Point out each malaria parasite.
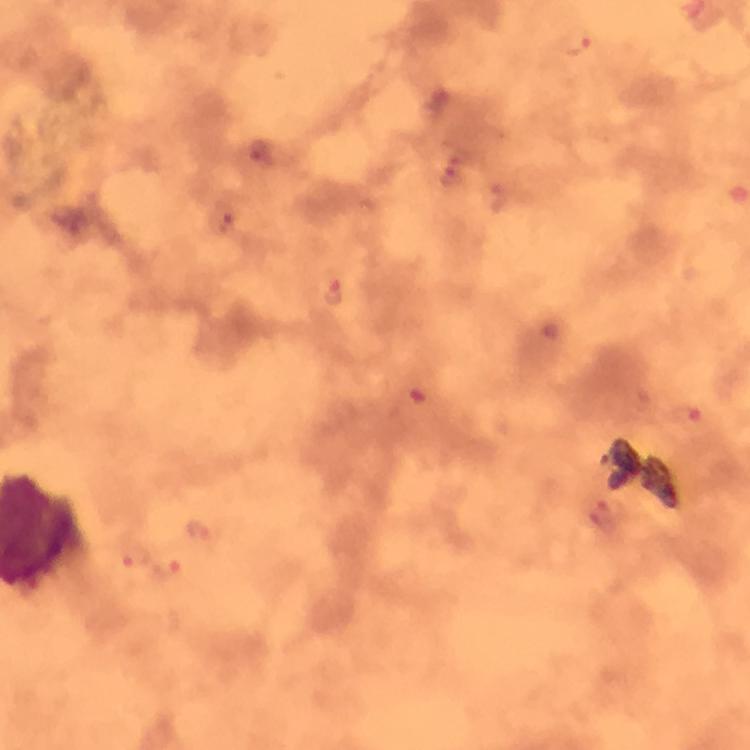

Approximate centers as [x, y] in pixels.
Malaria parasites: [578, 42], [261, 154], [454, 173], [499, 196], [222, 219], [334, 288], [552, 331], [420, 391], [686, 417], [198, 528], [133, 554], [168, 571].

cropped from = a single field of view
magnification = 100x
preparation = thick blood film
image size = 750×750 pixels
context = from a diagnostic examination for malaria
immersion oil = applied
capture = smartphone camera through the microscope
stain = Giemsa